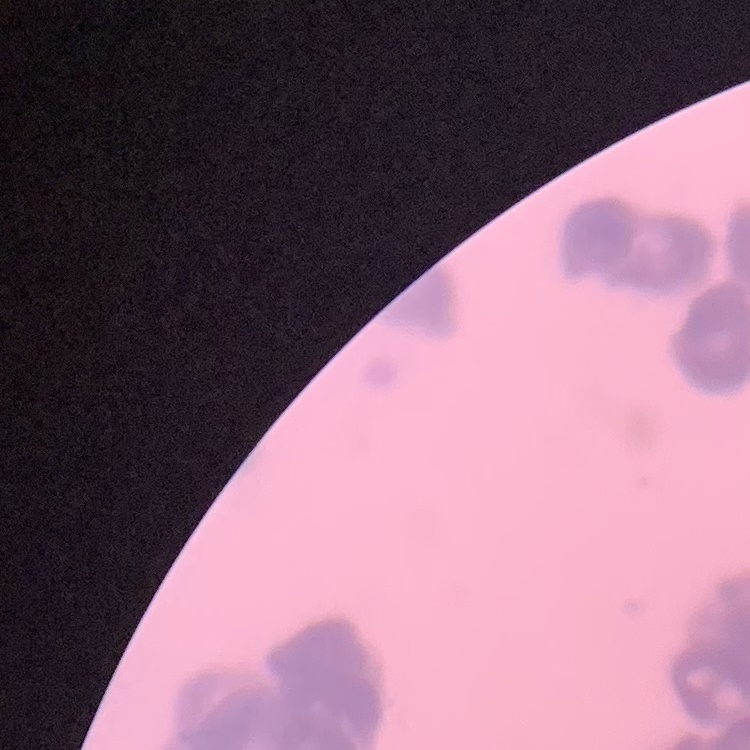
Summary:
  - Red blood cell morphology: rouleaux formation
  - Preparation: thin blood smear
  - Image type: square crop of a larger photomicrograph
  - Stain: Field's or Giemsa